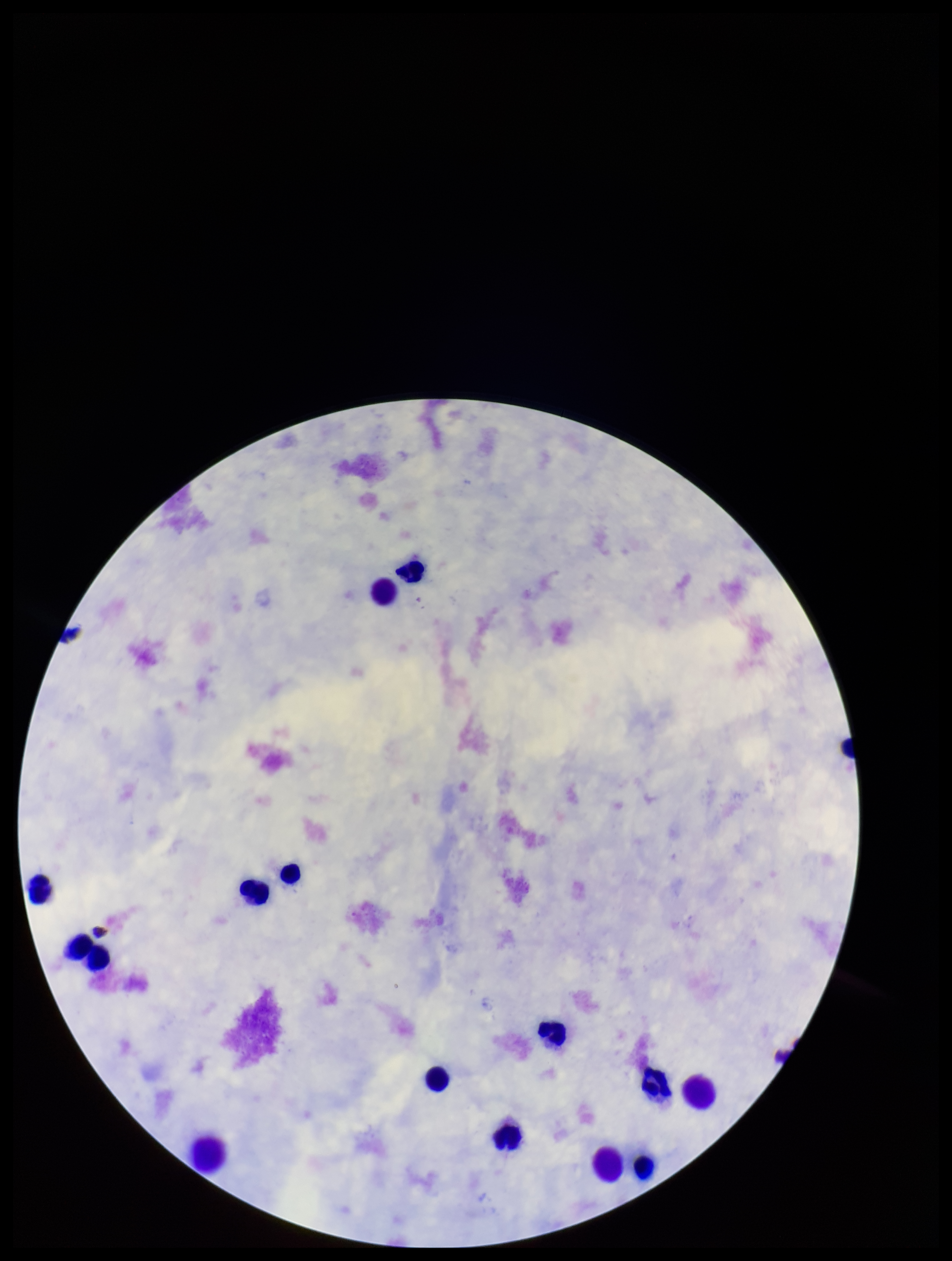 Patient malaria status: negative. Parasite count: 0. Plasmodium parasites: none identified. One field from this slide. Smartphone photograph taken through the eyepiece of a microscope. Leukocyte count: 15. Preparation: thick smear. Giemsa stain. Image is 952×1261 pixels.